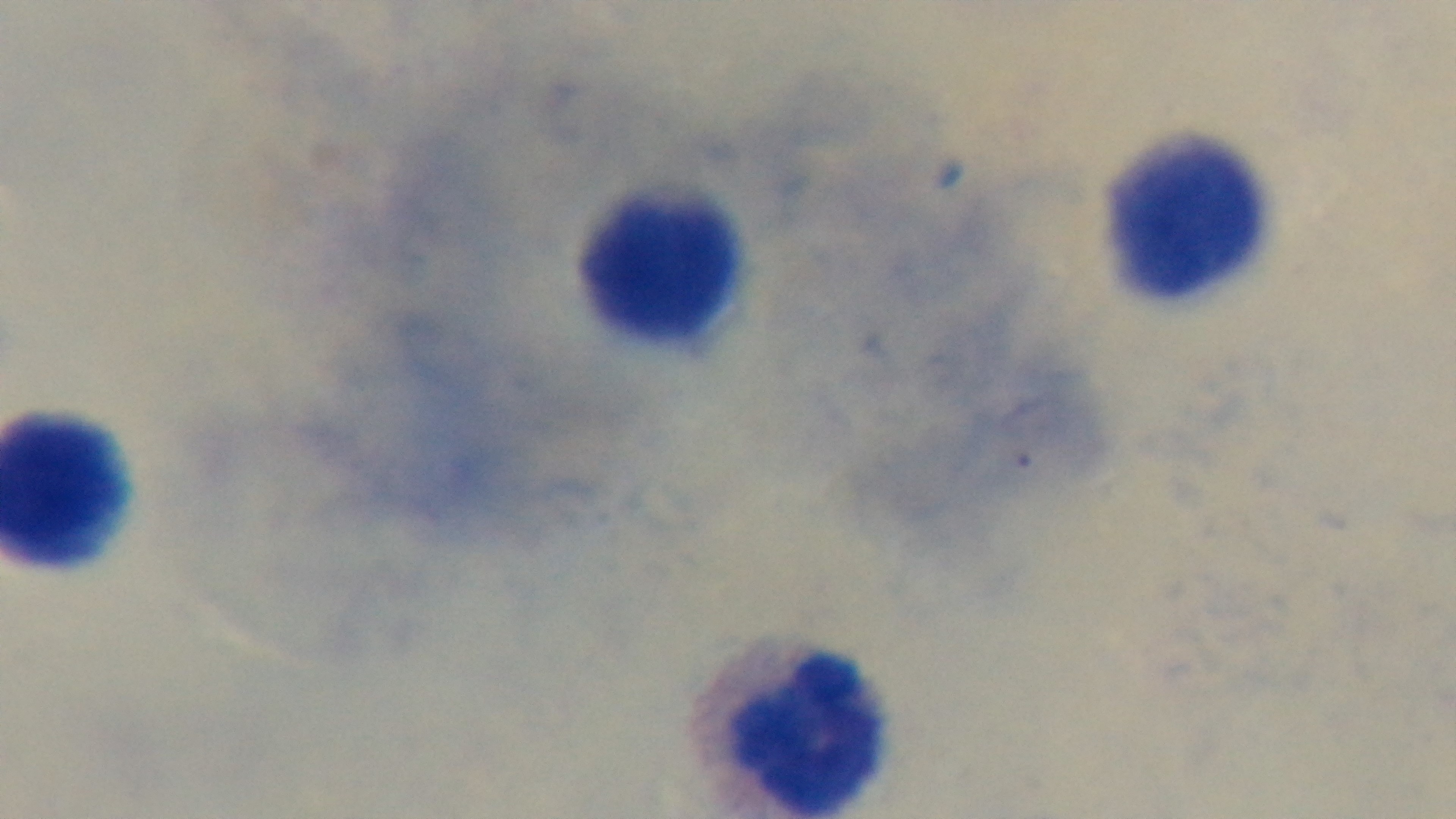 Captured with a mounted 4K digital camera. Malaria status: negative. Single field of view. Preparation: thick blood film. Light microscopy. Giemsa-stained. 100x oil-immersion objective.